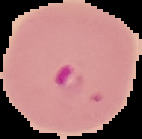
Summary:
  - Result: malaria parasites identified
  - Preparation: thin blood film
  - Image size: 142×139 pixels
  - Image type: segmented cell region with the area outside set to black